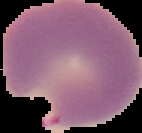
Summary:
  - Malaria status: parasitized
  - Preparation: thin blood smear
  - Image size: 142×133 pixels
  - Image type: segmented cell region with the area outside set to black